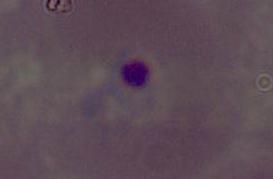 A Plasmodium parasite is shown. Photomicrograph. 400x or 1000x magnification.